Comment on the morphology of the red blood cells.
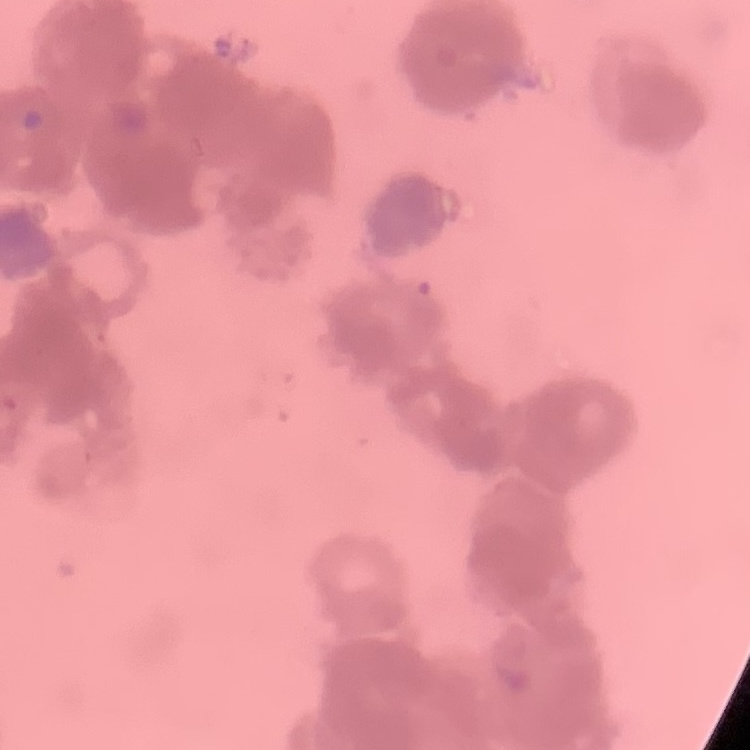

They show rouleaux formation.

Summary:
  - Stain: Field's or Giemsa
  - Preparation: thin blood smear
  - Image type: one tile cut from a larger photomicrograph